Locate and identify every blood parasite.
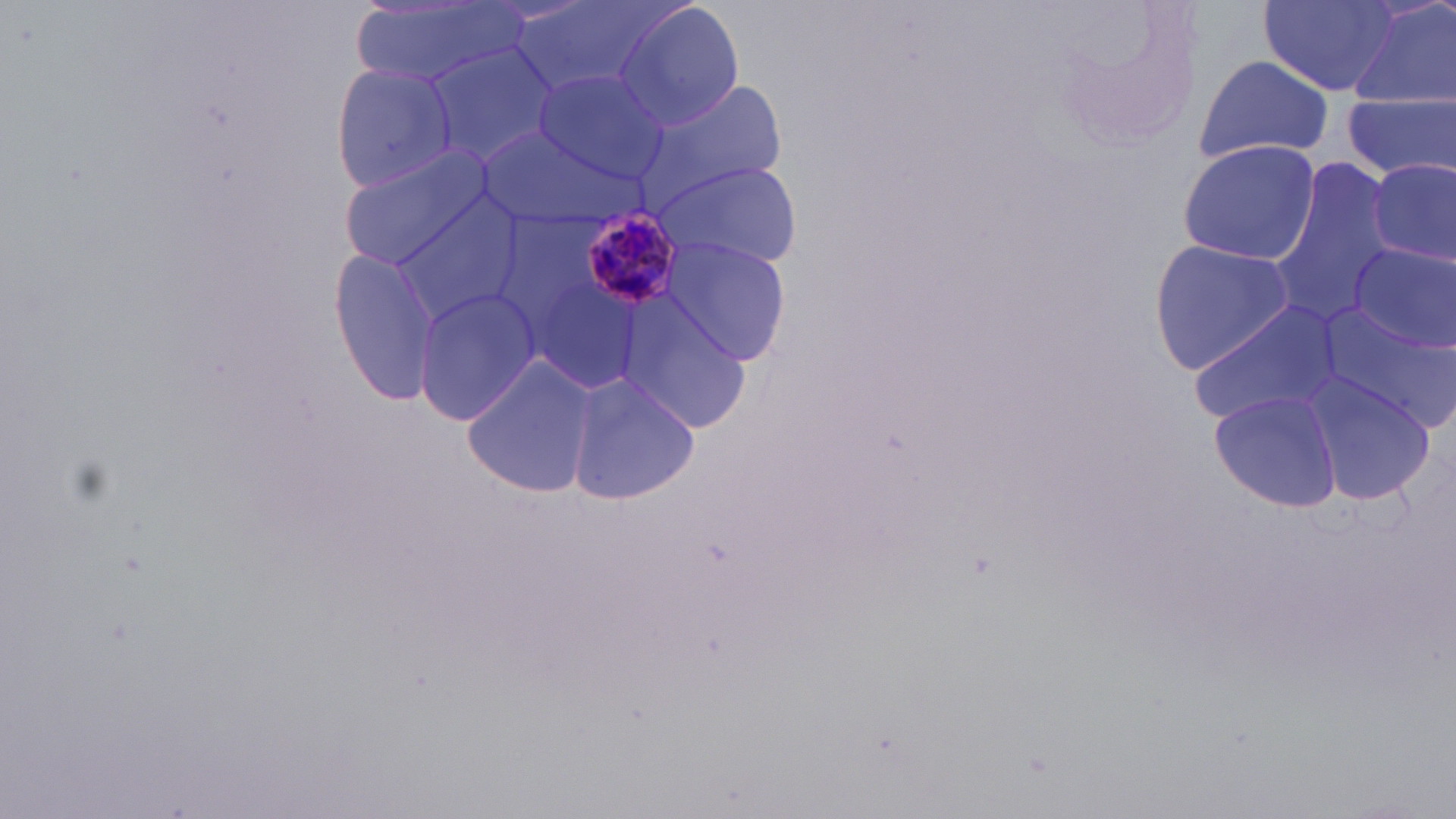

Approximate bounding boxes as (x1, y1, x2, y2) in pixels.
Plasmodium malariae-infected red blood cells: (579, 207, 686, 309).
No Plasmodium falciparum, Plasmodium ovale, Plasmodium vivax, Babesia divergens, or Trypanosoma brucei observed.

Summary:
  - Uninfected red blood cell locations: (350, 0, 520, 89), (511, 0, 681, 96), (613, 0, 744, 132), (1348, 0, 1456, 113), (1259, 2, 1401, 96), (419, 43, 556, 176), (1194, 55, 1332, 164), (329, 63, 456, 193), (532, 67, 672, 188), (638, 78, 790, 202), (1342, 90, 1453, 187), (474, 125, 638, 230), (1176, 138, 1321, 265), (338, 146, 494, 271), (651, 158, 804, 270), (1370, 159, 1455, 267), (1268, 162, 1398, 325), (383, 192, 529, 327), (659, 236, 796, 368), (1147, 240, 1297, 372), (1345, 247, 1455, 351), (330, 251, 443, 406), (413, 287, 541, 426), (617, 302, 751, 435), (1190, 302, 1342, 424), (1318, 305, 1456, 433), (462, 353, 597, 500), (565, 372, 701, 504), (1299, 373, 1438, 504), (1210, 391, 1343, 511)
  - Slide-level diagnosis: Plasmodium malariae
  - Image size: 1456×819 pixels
  - Field of view: single
  - Magnification: 1000x
  - Stain: May-Grünwald-Giemsa
  - Modality: light microscopy
  - Preparation: thin blood film